Mark where platelets are.
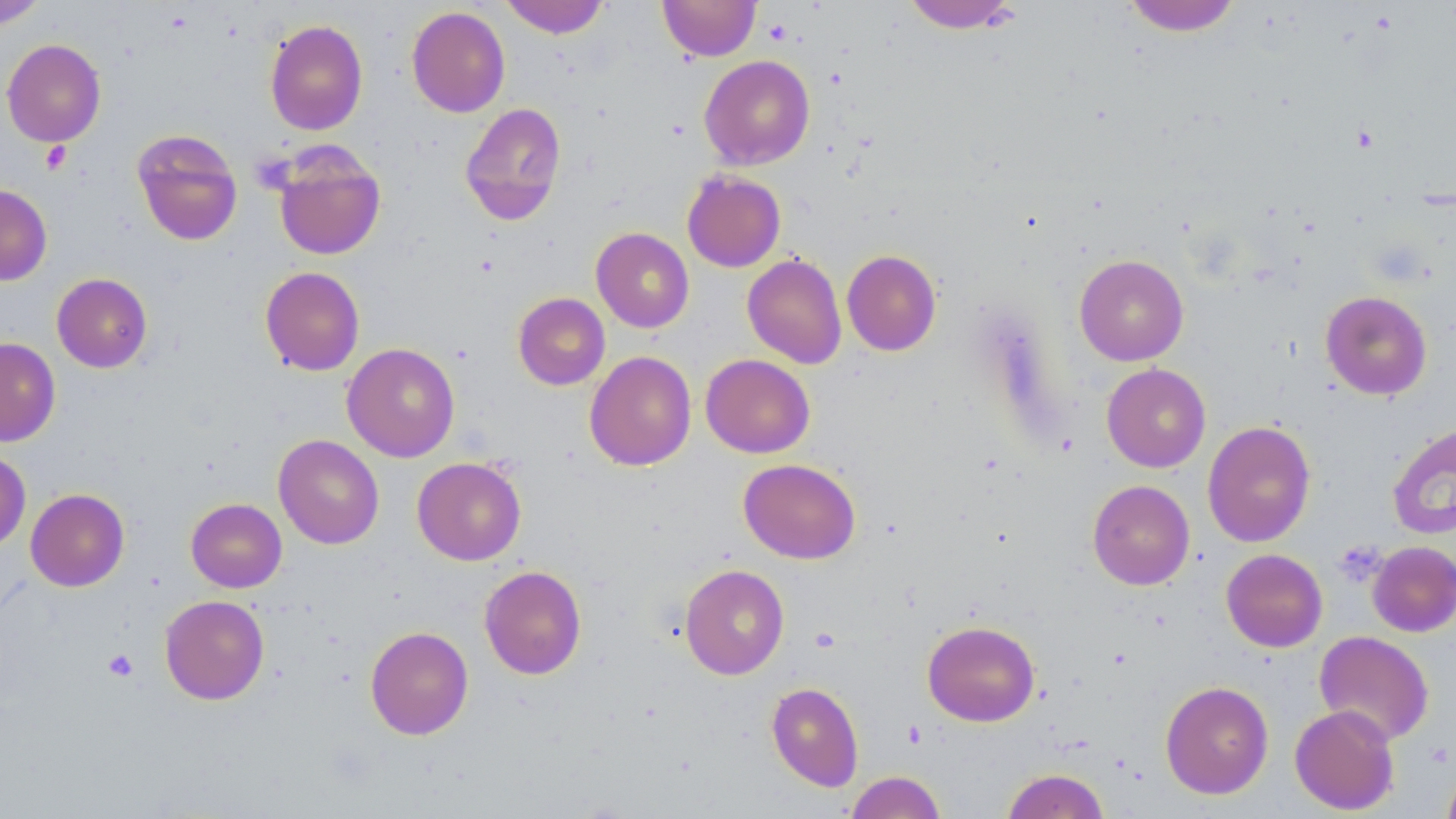

Approximate bounding boxes as (x1, y1, x2, y2) in pixels.
Platelets: (764, 19, 792, 45), (1352, 124, 1379, 153), (40, 141, 72, 174), (103, 649, 138, 681), (1428, 742, 1454, 767).

Summary:
  - Uninfected red blood cell locations: (0, 0, 47, 28), (500, 0, 610, 38), (658, 0, 761, 61), (901, 0, 1022, 34), (1123, 0, 1242, 36), (406, 6, 510, 117), (264, 19, 368, 136), (1, 38, 106, 147), (699, 55, 815, 170), (460, 102, 566, 226), (131, 128, 243, 245), (271, 143, 386, 261), (682, 169, 786, 272), (0, 184, 53, 285), (591, 227, 694, 333), (842, 249, 941, 355), (742, 253, 847, 369), (1074, 254, 1189, 366), (260, 266, 365, 376), (51, 273, 153, 373), (1320, 291, 1432, 400), (513, 292, 610, 390), (0, 337, 60, 447), (342, 342, 460, 462), (584, 351, 697, 471), (701, 354, 815, 458), (1101, 363, 1211, 472), (1202, 420, 1316, 548), (1387, 422, 1456, 540), (273, 434, 384, 550), (0, 449, 31, 551), (412, 457, 526, 565), (738, 459, 861, 564), (1087, 480, 1195, 590), (25, 488, 129, 591), (186, 498, 287, 593), (1368, 541, 1456, 637), (1221, 548, 1327, 652), (679, 564, 790, 679), (479, 565, 587, 680), (160, 595, 269, 705), (922, 620, 1040, 727), (365, 626, 474, 740), (1314, 631, 1434, 745), (1160, 680, 1274, 798), (766, 681, 864, 791), (1290, 704, 1400, 815), (1441, 764, 1456, 819), (1002, 768, 1109, 819), (845, 771, 946, 819)
  - Slide-level diagnosis: negative for blood parasites
  - Preparation: thin blood film
  - Magnification: 1000x
  - Modality: light microscopy
  - Image size: 1456×819 pixels
  - Field of view: single
  - Stain: May-Grünwald-Giemsa